Name the parasite shown.
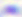
This is Toxoplasma gondii.

Summary:
  - Modality: micrograph
  - Magnification: 400x